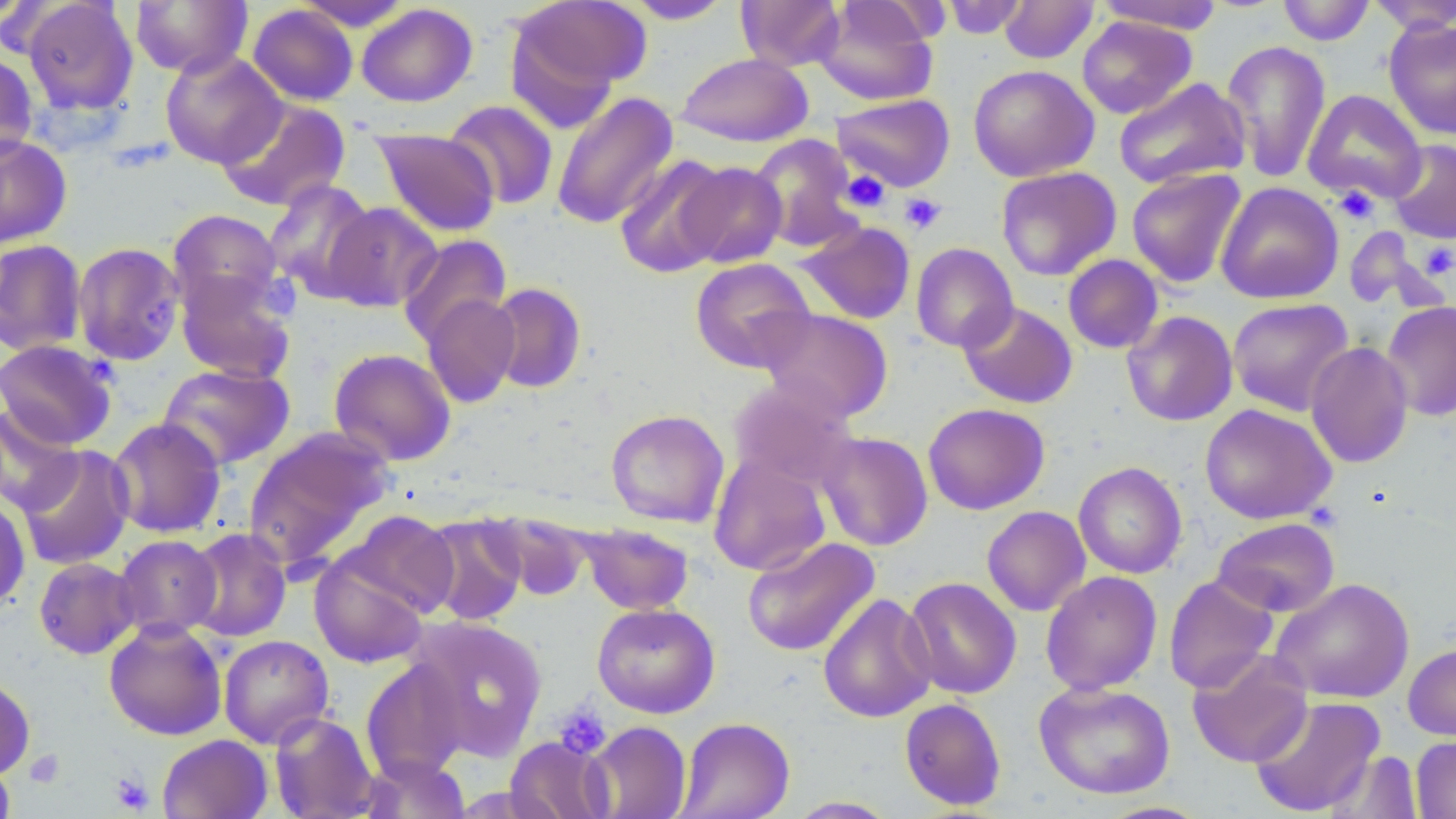
Summary:
  - Coordinate format: approximate bounding boxes as [x1, y1, x2, y2] in pixels
  - Uninfected red blood cell locations: [0, 0, 44, 30], [21, 0, 139, 117], [130, 0, 252, 77], [510, 0, 649, 102], [736, 0, 845, 72], [939, 0, 1031, 39], [1095, 0, 1221, 32], [1277, 0, 1375, 46], [1367, 0, 1456, 33], [294, 1, 413, 31], [623, 1, 734, 24], [815, 1, 939, 106], [998, 1, 1099, 64], [356, 3, 477, 107], [247, 4, 358, 106], [1076, 16, 1197, 119], [1384, 18, 1456, 140], [1221, 39, 1331, 183], [159, 50, 287, 168], [0, 52, 39, 163], [676, 52, 813, 147], [968, 64, 1099, 181], [1113, 77, 1251, 190], [1302, 89, 1427, 205], [551, 91, 678, 229], [832, 94, 955, 192], [216, 98, 351, 212], [444, 100, 559, 210], [373, 128, 501, 237], [0, 133, 72, 250], [748, 134, 863, 252], [1387, 139, 1456, 244], [613, 154, 732, 278], [679, 161, 786, 268], [996, 166, 1121, 281], [1126, 168, 1247, 288], [264, 179, 378, 300], [1215, 181, 1343, 304], [324, 202, 442, 312], [167, 209, 285, 319], [798, 220, 917, 325], [397, 234, 511, 347], [0, 239, 87, 356], [72, 241, 186, 366], [910, 242, 1018, 352], [1062, 254, 1164, 354], [690, 257, 815, 372], [176, 270, 296, 384], [486, 283, 587, 393], [421, 293, 521, 408], [1228, 298, 1354, 416], [958, 301, 1078, 409], [1381, 301, 1456, 422], [756, 308, 894, 424], [1122, 311, 1238, 426], [0, 339, 117, 450], [1305, 341, 1414, 468], [329, 347, 456, 466], [157, 363, 294, 470], [728, 379, 858, 493], [922, 402, 1050, 515], [0, 404, 83, 516], [1199, 404, 1337, 525], [606, 409, 730, 528], [107, 417, 227, 538], [243, 427, 395, 572], [816, 431, 934, 551], [16, 444, 135, 570], [708, 453, 831, 576], [1073, 461, 1187, 579], [0, 493, 31, 612], [981, 506, 1091, 617], [340, 510, 460, 618], [483, 510, 592, 601], [420, 514, 528, 626], [1212, 517, 1340, 617], [579, 523, 695, 615], [184, 528, 292, 643], [113, 535, 222, 640], [742, 536, 880, 657], [309, 555, 429, 669], [33, 557, 140, 660], [1040, 570, 1162, 696], [1163, 575, 1279, 693], [903, 577, 1022, 699], [1269, 578, 1415, 704], [818, 592, 938, 723], [591, 602, 720, 718], [407, 615, 547, 761], [103, 619, 228, 741], [218, 634, 334, 748], [1403, 642, 1456, 741], [1187, 650, 1314, 767], [360, 659, 468, 782], [0, 674, 36, 781], [1033, 681, 1176, 799], [1249, 695, 1385, 817], [899, 697, 1007, 810], [269, 711, 379, 819], [676, 716, 795, 819], [582, 721, 691, 819], [157, 734, 272, 819], [1411, 735, 1456, 819], [504, 736, 613, 819], [1325, 750, 1423, 818], [0, 755, 16, 818], [357, 755, 471, 818], [787, 796, 899, 818], [1095, 801, 1213, 819]
  - Platelet locations: [839, 170, 890, 213], [1334, 186, 1379, 224], [900, 193, 946, 235], [1420, 243, 1456, 279], [260, 275, 300, 320], [553, 705, 611, 759], [24, 749, 65, 787], [110, 771, 155, 814]
  - Slide-level diagnosis: negative for blood parasites
  - Field of view: one of a larger specimen
  - Stain: May-Grünwald-Giemsa
  - Preparation: thin blood smear
  - Modality: light microscopy
  - Magnification: 1000x
  - Image size: 1456×819 pixels